Point out each malaria parasite and each leukocyte.
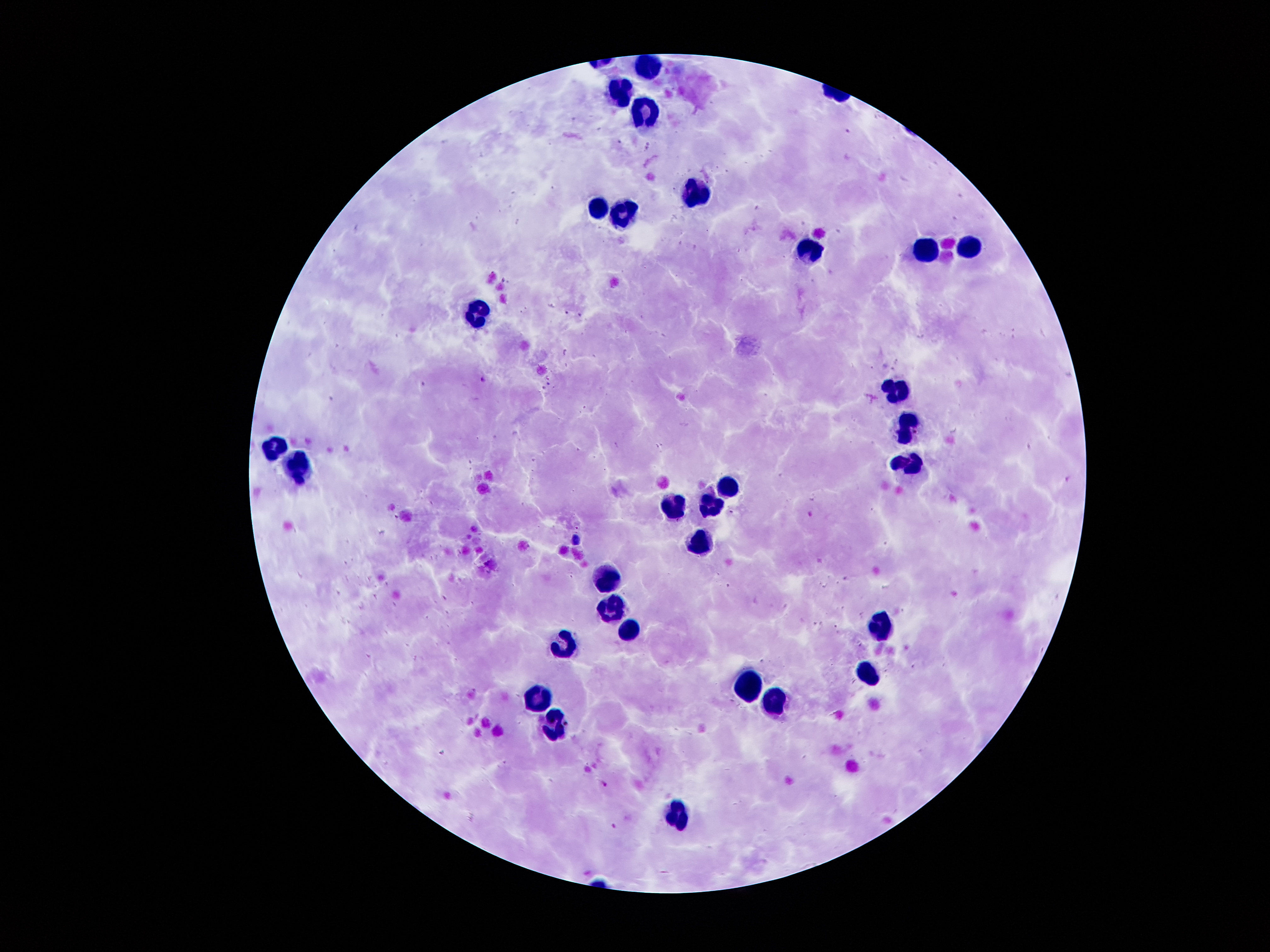

Approximate centers as (x, y) in pixels.
Malaria parasites: (568, 312), (581, 316), (482, 379), (550, 383), (543, 387), (1067, 480), (731, 512), (811, 514), (396, 517), (577, 528), (604, 784), (613, 827).
Leukocytes: (649, 61), (621, 86), (644, 113), (694, 195), (595, 204), (626, 213), (968, 245), (924, 249), (812, 251), (477, 310), (898, 388), (908, 425), (272, 450), (910, 459), (301, 466), (728, 483), (711, 504), (673, 509), (701, 542), (605, 575), (605, 603), (881, 622), (625, 625), (565, 645), (869, 669), (750, 679), (776, 697), (537, 699), (551, 721), (675, 810).

patient malaria status = positive for Plasmodium falciparum
magnification = 100x
capture = smartphone through the microscope eyepiece
image size = 1270×952 pixels
preparation = thick peripheral-blood smear
field of view = one from this slide
stain = Giemsa